Point out each Plasmodium parasite.
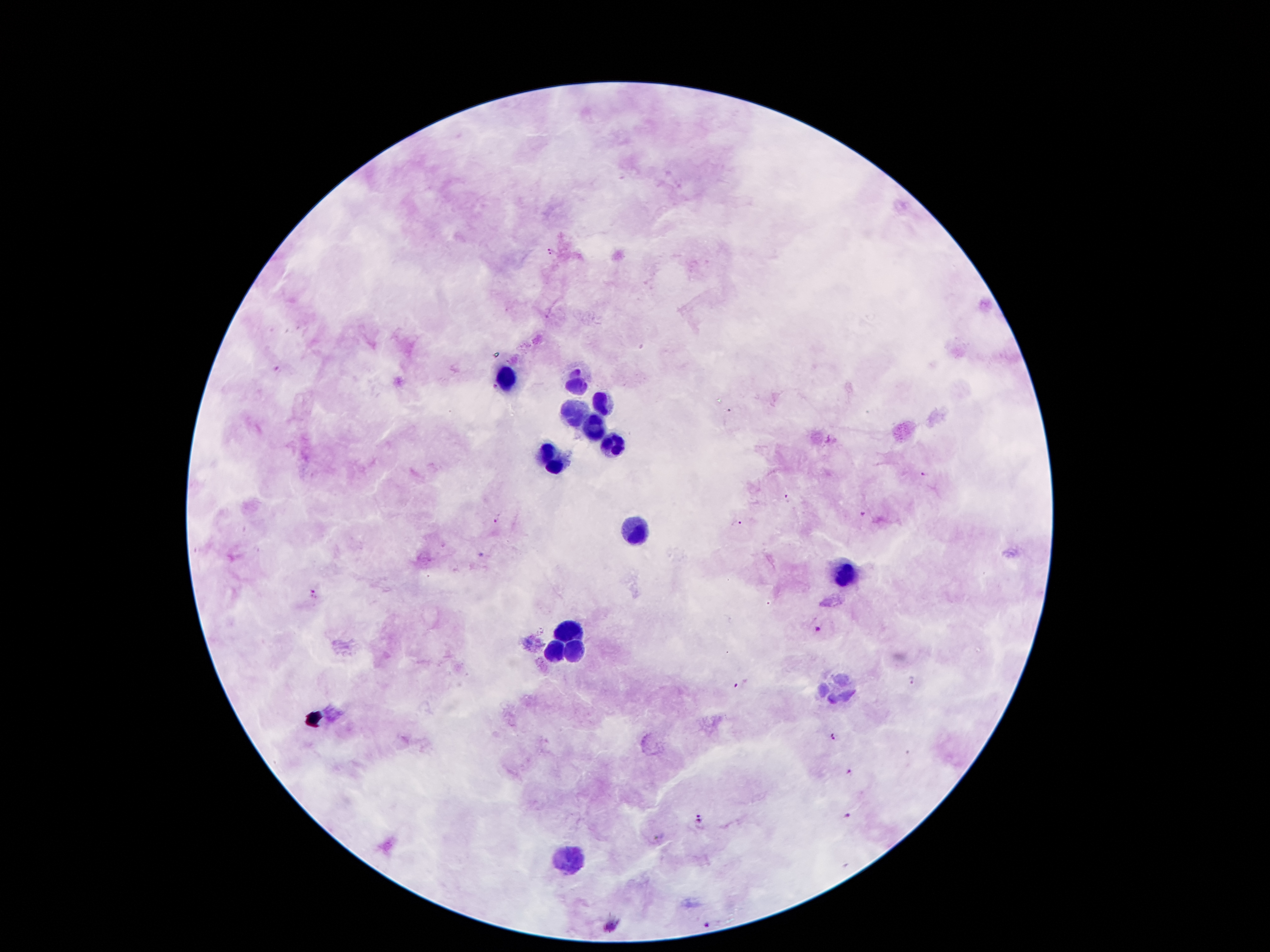
Approximate centers as (x, y) in pixels.
Plasmodium parasites: (552, 251), (577, 372), (495, 388), (923, 473), (788, 496), (864, 515), (498, 520), (735, 523), (314, 594), (816, 629), (912, 680), (741, 684), (836, 737), (848, 773), (847, 812), (698, 818), (707, 923).

Leukocyte locations: (510, 378), (576, 385), (604, 399), (576, 411), (590, 425), (611, 441), (552, 457), (632, 527), (844, 572), (569, 630), (571, 646), (557, 651), (839, 690), (569, 858). Thick blood film. Single field of view. Giemsa-stained preparation. Image is 1270×952 pixels. Smartphone photograph taken through the microscope eyepiece. 100x magnification. Patient malaria status: positive for Plasmodium falciparum.